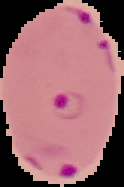
Malaria status: parasitized. Cell region segmented out of the field of view; the surrounding area is masked to black. From a thin blood smear. Image is 124×187 pixels.